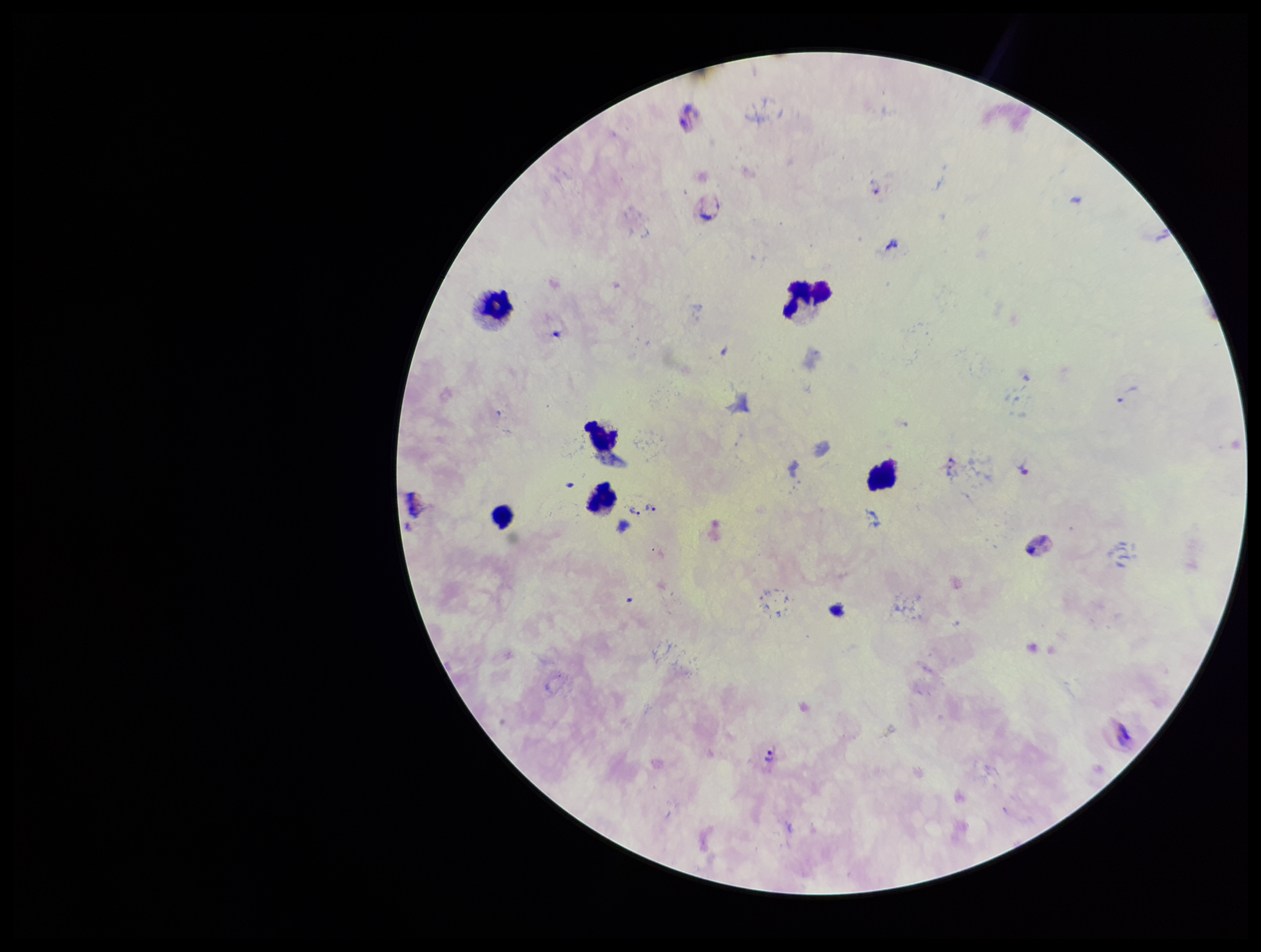

parasite count = 10
Plasmodium parasites = seen
stain = Giemsa
capture = smartphone photograph through the microscope eyepiece
patient malaria status = infected
leukocyte count = 6
preparation = thick smear
field of view = one from this slide
species reported for this patient = Plasmodium vivax
image size = 1261×952 pixels